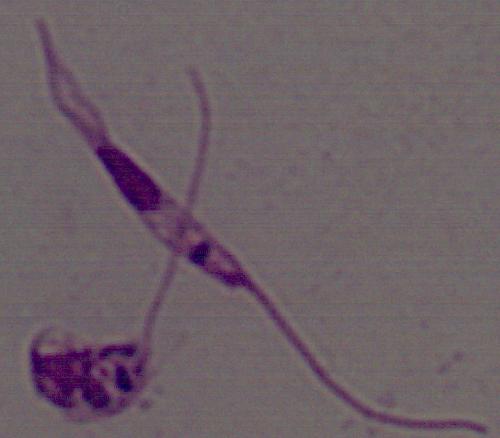 A Leishmania parasite is shown. Photomicrograph. 1000x magnification.